Name the parasite shown.
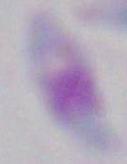
Toxoplasma gondii.

Summary:
  - Modality: photomicrograph
  - Magnification: 1000x